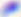

{
  "identification": "Toxoplasma gondii",
  "modality": "micrograph",
  "magnification": "400x"
}